Identify the parasite.
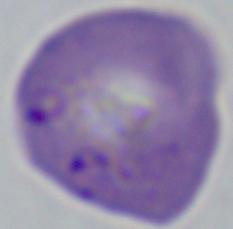

This is Babesia.

{
  "modality": "micrograph",
  "magnification": "1000x"
}